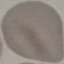
Summary:
  - Result: no malaria parasites detected
  - Preparation: thin smear
  - Stain: Giemsa
  - Capture: smartphone through the microscope eyepiece
  - Image type: cell patch, automatically extracted from a larger field of view and resized to 64 × 64 pixels